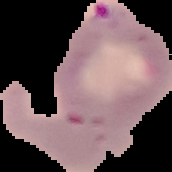

Cell region segmented out of the field of view; the surrounding area is masked to black. Image is 172×172 pixels. From a thin blood film. Result: Plasmodium parasites identified.